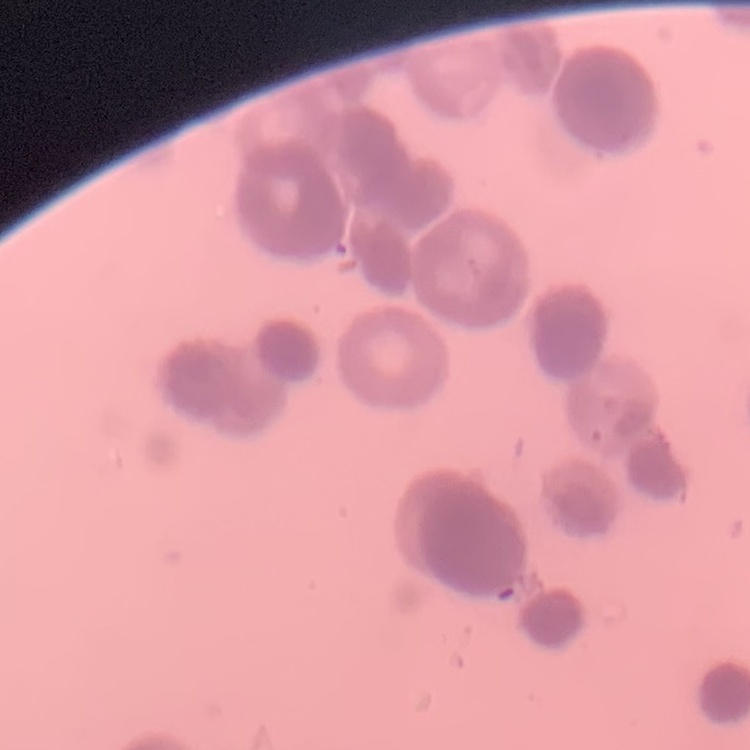
Summary:
  - Erythrocyte morphology: rouleaux formation
  - Image type: square crop of a larger photomicrograph
  - Stain: Field's or Giemsa
  - Preparation: thin peripheral smear